Point out each malaria parasite.
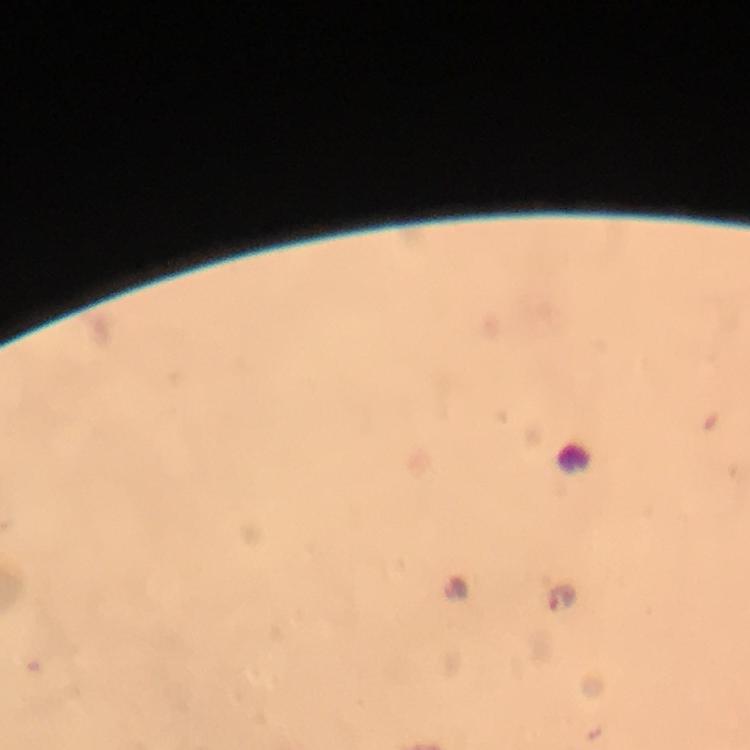
Approximate centers as {x, y} in pixels.
Malaria parasites: {560, 599}.

Image is 750×750 pixels. Smartphone photograph taken through a microscope. Cropped region of a single field of view. Thick blood smear. Giemsa stain. From a malaria diagnostic workup. Immersion oil was used. At 100x magnification.